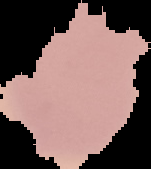
image_type: cell region segmented out of the field of view; surrounding area masked to black
image_size: 151×169 pixels
preparation: thin blood film
result: no malaria parasites seen